State which parasite is depicted.
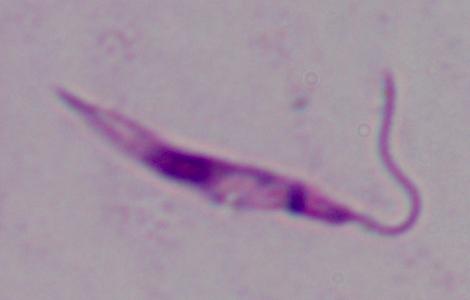
Leishmania.

{
  "modality": "micrograph",
  "magnification": "1000x"
}